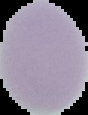

{
  "preparation": "thin blood smear",
  "image_size": "88×115 pixels",
  "image_type": "segmented cell region on a black background",
  "malaria_status": "uninfected"
}